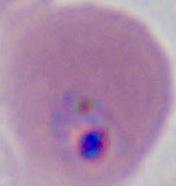

Summary:
  - Modality: photomicrograph
  - Magnification: 400x or 1000x
  - Identification: Plasmodium